Identify the parasite.
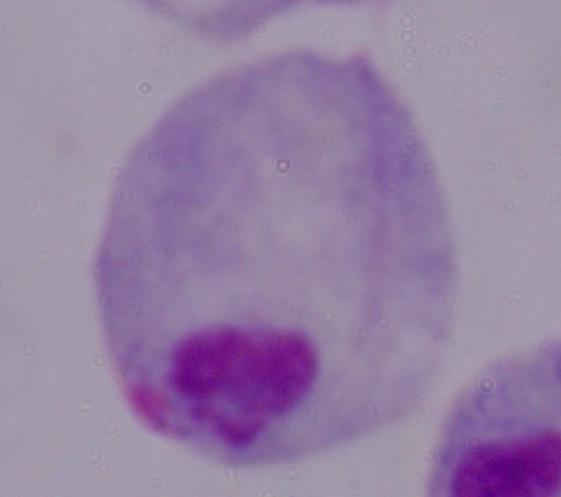
This is a trichomonad.

1000x magnification. Micrograph.